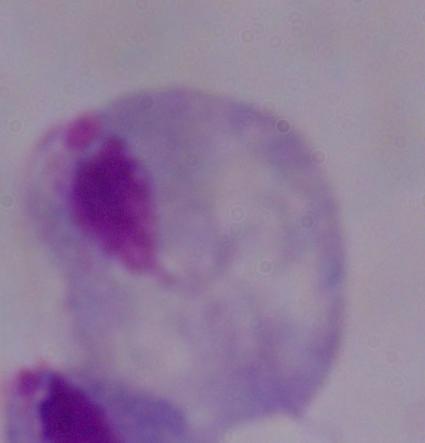 Photomicrograph. A trichomonad is shown. 1000x magnification.